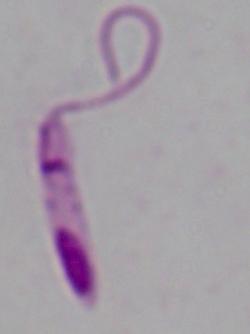

identification = Leishmania
modality = photomicrograph
magnification = 1000x